Assess for Plasmodium parasites.
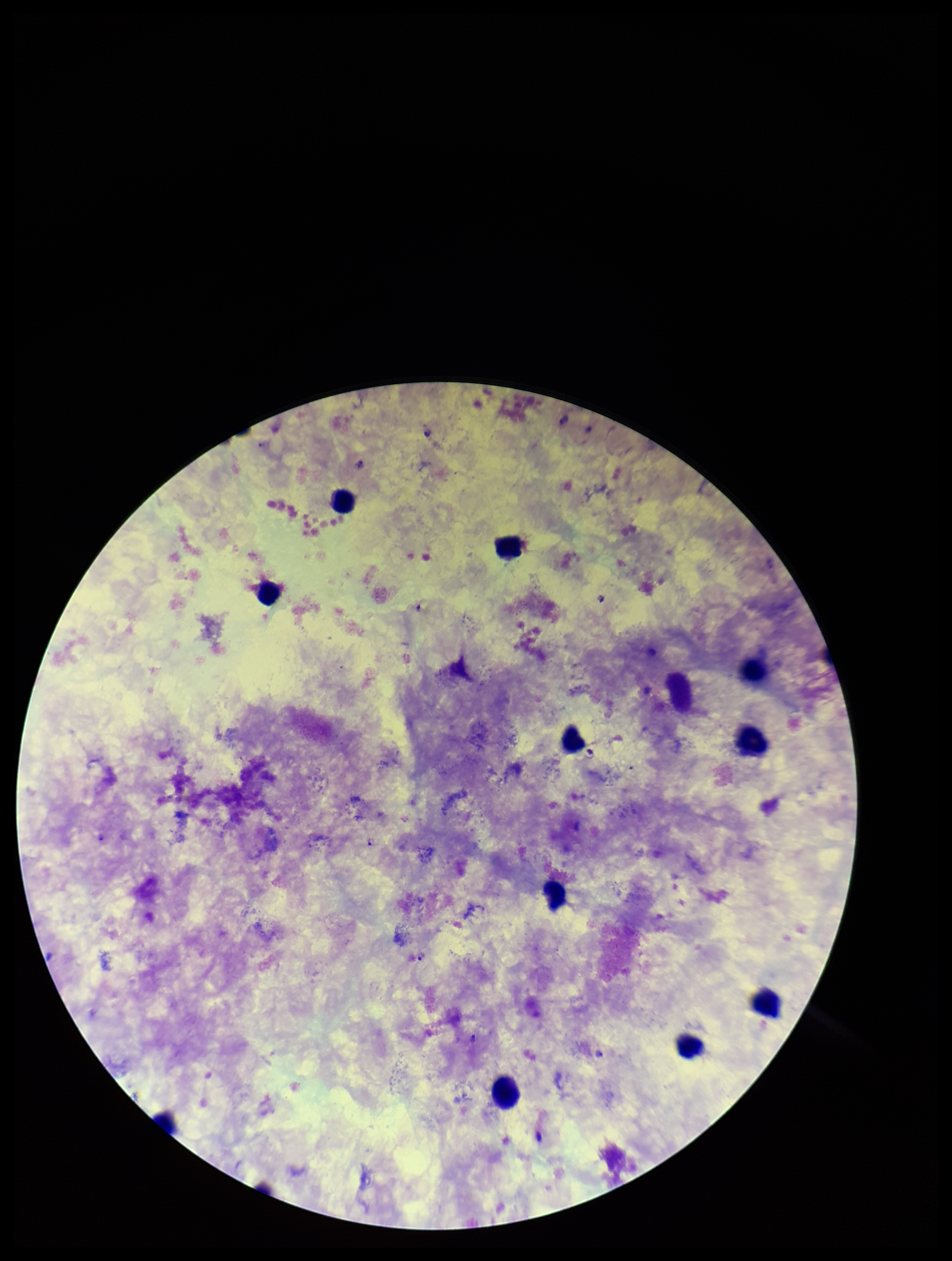

Seen.

Species reported for this patient: Plasmodium falciparum. Stained with Giemsa. Leukocyte count: 11. Image is 952×1261 pixels. Preparation: thick smear. Patient malaria status: infected. Parasite count: 8. One field from this slide. Smartphone photograph taken through the eyepiece of a microscope.